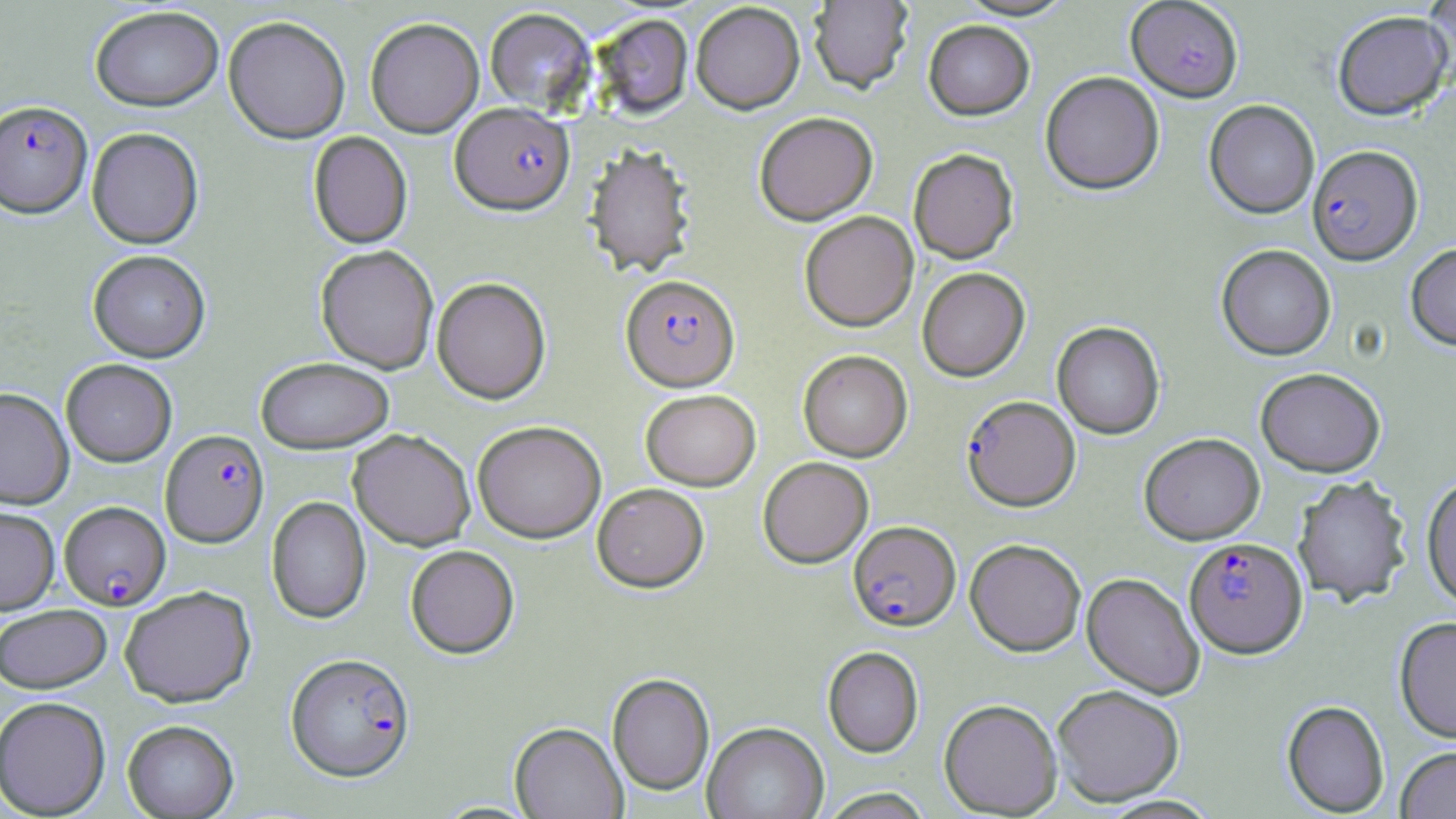

Summary:
  - Coordinate format: approximate bounding boxes as [x1, y1, x2, y2] in pixels
  - Plasmodium falciparum-infected red blood cell locations (subset): [0, 103, 93, 223], [449, 105, 575, 221], [1307, 147, 1423, 268], [620, 278, 741, 396], [961, 397, 1080, 514], [159, 431, 270, 551], [59, 502, 171, 612], [848, 523, 961, 634], [1183, 539, 1308, 661], [285, 655, 415, 784]
  - Uninfected red blood cell locations (subset): [809, 0, 913, 97], [955, 0, 1077, 22], [1424, 0, 1456, 82], [691, 4, 805, 119], [90, 8, 225, 115], [484, 10, 598, 115], [1332, 12, 1453, 122], [593, 16, 693, 122], [223, 18, 350, 147], [365, 20, 484, 141], [923, 22, 1035, 124], [1040, 73, 1164, 197], [1204, 100, 1319, 220], [755, 116, 878, 229], [86, 130, 204, 252], [308, 133, 413, 251], [583, 147, 697, 281], [908, 151, 1019, 266], [800, 214, 919, 334], [1406, 243, 1456, 353], [1216, 245, 1336, 361], [315, 248, 438, 376], [87, 253, 210, 364], [917, 269, 1030, 383], [431, 279, 552, 407], [1052, 323, 1165, 440], [797, 352, 913, 464], [256, 360, 394, 455], [1255, 370, 1386, 478], [0, 390, 74, 510], [641, 392, 761, 493], [472, 424, 606, 546], [348, 431, 476, 552], [1140, 434, 1264, 545], [758, 459, 873, 571], [1293, 477, 1411, 608], [1420, 478, 1456, 613], [592, 485, 709, 595], [266, 497, 371, 625], [0, 508, 60, 616], [964, 540, 1086, 658], [405, 547, 519, 660], [1081, 574, 1205, 700], [120, 589, 257, 708], [0, 606, 112, 694], [1394, 619, 1456, 745], [822, 647, 924, 759], [607, 675, 714, 797], [1052, 687, 1185, 807], [0, 697, 111, 817], [939, 700, 1062, 817], [1281, 702, 1389, 816], [122, 721, 239, 818], [510, 723, 627, 819], [703, 723, 827, 819], [1395, 748, 1456, 818], [818, 788, 934, 819]
  - Slide-level diagnosis: Plasmodium falciparum
  - Modality: light microscopy
  - Preparation: thin blood film
  - Stain: May-Grünwald-Giemsa
  - Magnification: 1000x
  - Field of view: one of a larger specimen
  - Image size: 1456×819 pixels